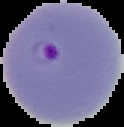
Summary:
  - Image type: segmented cell region with the area outside set to black
  - Preparation: thin blood film
  - Image size: 124×127 pixels
  - Malaria status: parasitized